Identify the blood parasite species.
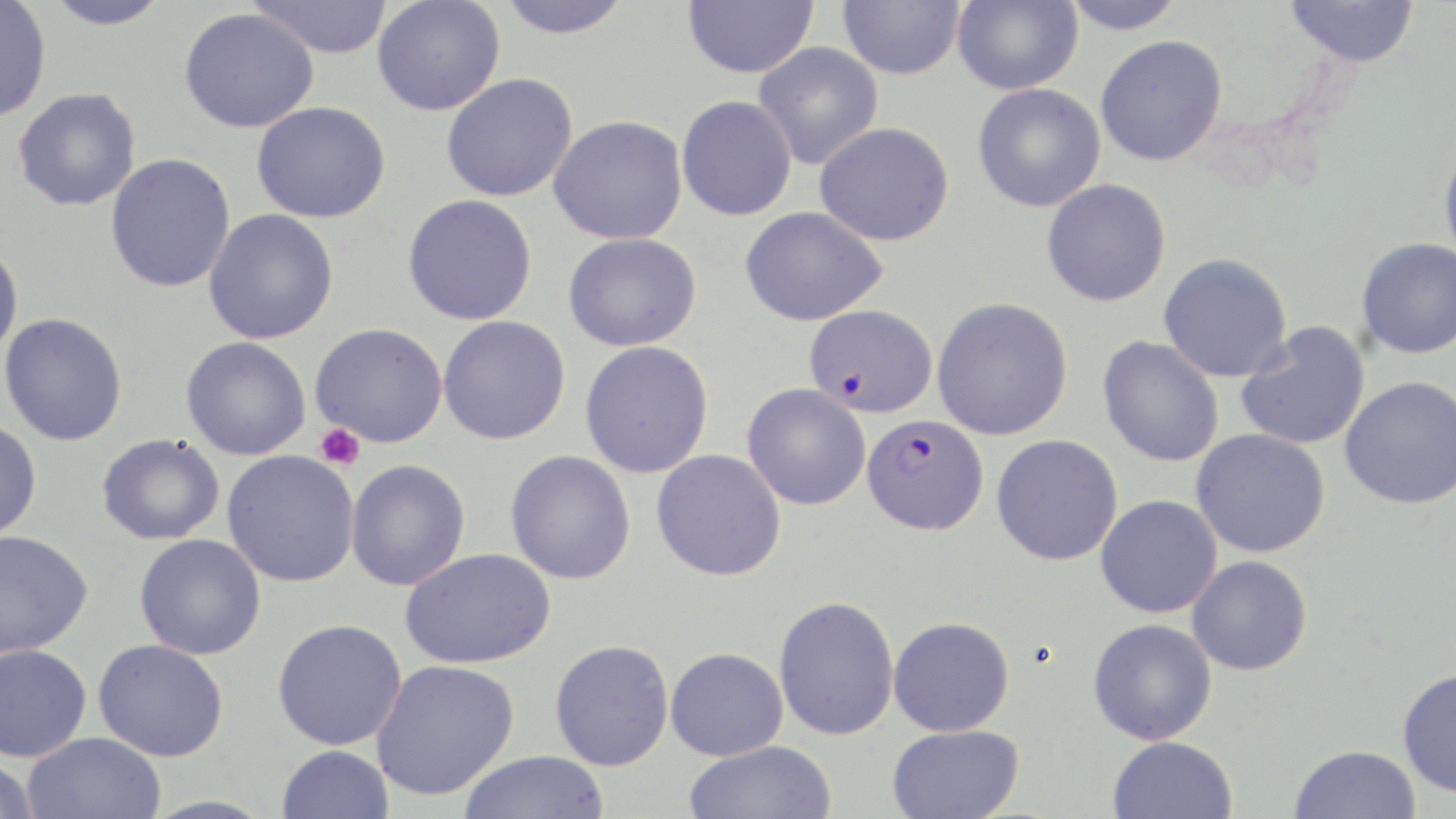
Plasmodium falciparum.

Summary:
  - Coordinate format: approximate bounding boxes as [x1, y1, x2, y2] in pixels
  - Platelet locations: [314, 423, 365, 470]
  - Plasmodium falciparum-infected red blood cell locations: [804, 304, 938, 419], [861, 413, 988, 536]
  - Uninfected red blood cell locations: [0, 0, 51, 123], [44, 0, 171, 30], [248, 0, 393, 59], [372, 0, 505, 116], [496, 0, 634, 39], [683, 0, 819, 79], [839, 0, 964, 79], [952, 0, 1082, 95], [1060, 0, 1187, 34], [1285, 0, 1420, 67], [179, 8, 319, 133], [1095, 34, 1228, 166], [753, 42, 883, 169], [441, 73, 578, 202], [973, 83, 1106, 212], [13, 88, 141, 211], [676, 95, 797, 221], [251, 101, 390, 223], [549, 115, 688, 245], [815, 122, 955, 246], [1438, 142, 1456, 268], [105, 153, 236, 293], [1041, 178, 1171, 307], [402, 194, 538, 325], [741, 206, 887, 327], [203, 209, 339, 345], [563, 232, 702, 352], [1357, 237, 1456, 359], [0, 239, 23, 362], [1158, 252, 1294, 382], [932, 297, 1073, 440], [0, 313, 128, 446], [438, 315, 571, 445], [1236, 322, 1371, 450], [310, 323, 448, 447], [181, 336, 311, 460], [1097, 336, 1224, 467], [580, 340, 714, 478], [1340, 375, 1456, 509], [742, 383, 871, 510], [0, 420, 42, 542], [1191, 429, 1330, 558], [97, 433, 225, 545], [992, 434, 1123, 566], [651, 449, 786, 580], [505, 450, 636, 585], [222, 451, 360, 587], [346, 459, 471, 591], [1096, 495, 1222, 619], [0, 530, 93, 658], [134, 533, 266, 659], [400, 547, 556, 669], [1186, 555, 1312, 676], [773, 595, 900, 741], [889, 616, 1015, 736], [272, 618, 407, 750], [1088, 618, 1217, 745], [92, 638, 229, 762], [549, 639, 674, 771], [0, 644, 92, 762], [665, 647, 788, 761], [372, 659, 520, 801], [1397, 667, 1456, 797], [887, 724, 1024, 819], [22, 731, 165, 819], [1107, 735, 1238, 819], [684, 740, 837, 819], [276, 744, 394, 819], [1289, 744, 1421, 819], [457, 751, 611, 818], [0, 756, 40, 819]
  - Image size: 1456×819 pixels
  - Magnification: 1000x
  - Field of view: single
  - Preparation: thin blood smear
  - Stain: May-Grünwald-Giemsa
  - Modality: optical microscopy